State which cell type is depicted.
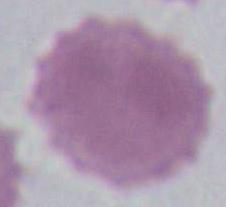
This is an erythrocyte.

Summary:
  - Magnification: 1000x
  - Modality: photomicrograph